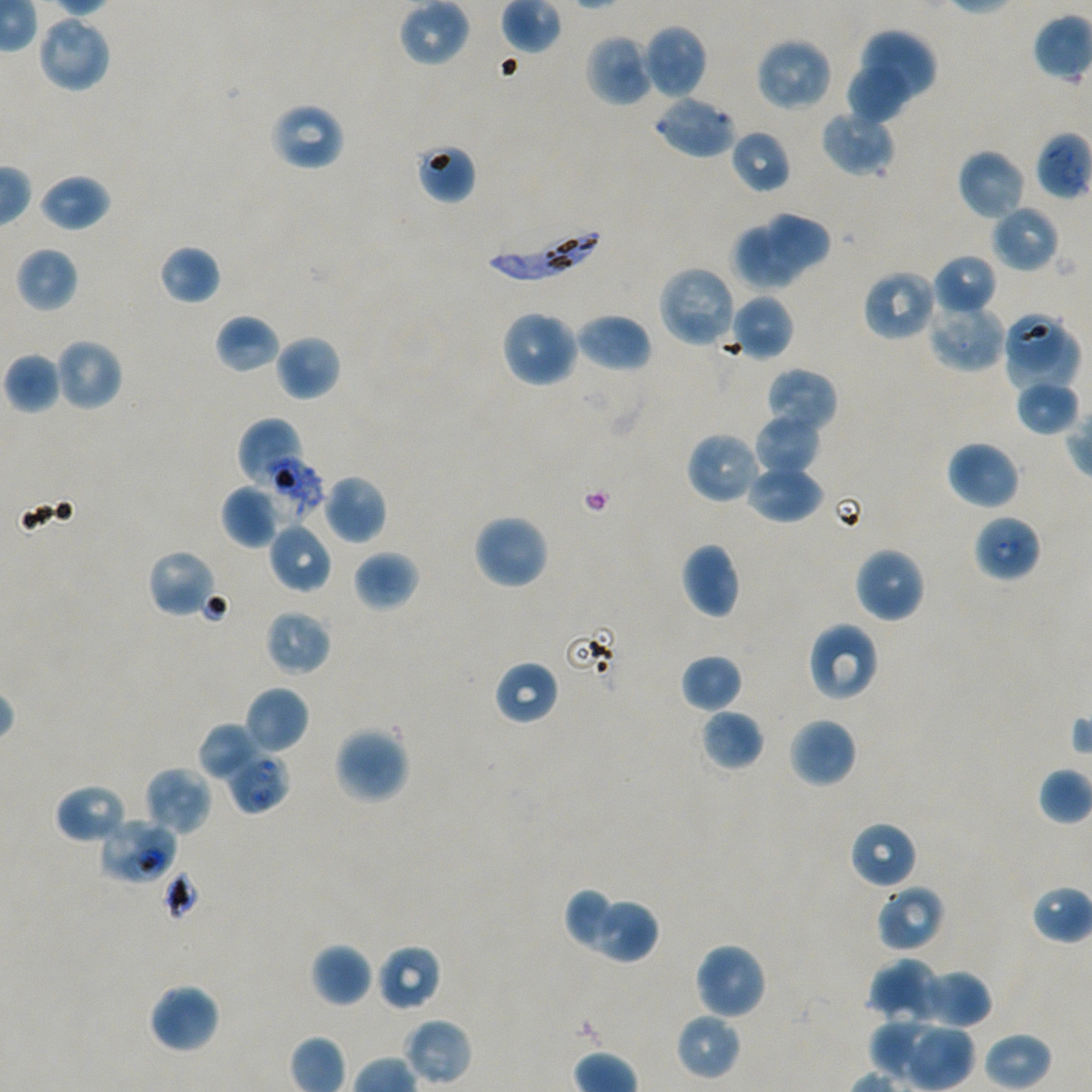
Approximate bounding rectangles given as corner coordinates in pixels from the top-left. Not every red blood cell is marked. Locations of red blood cells of indeterminate infection status: (x1=255, y1=448, x2=325, y2=522), (x1=973, y1=513, x2=1042, y2=583), (x1=227, y1=751, x2=290, y2=814), (x1=98, y1=816, x2=177, y2=885), (x1=162, y1=869, x2=202, y2=923). Locations of uninfected red blood cells: (x1=399, y1=0, x2=471, y2=67), (x1=35, y1=13, x2=113, y2=94), (x1=642, y1=24, x2=708, y2=100), (x1=856, y1=28, x2=937, y2=106), (x1=584, y1=33, x2=655, y2=108), (x1=754, y1=37, x2=833, y2=113), (x1=845, y1=58, x2=913, y2=125), (x1=653, y1=94, x2=738, y2=160), (x1=269, y1=101, x2=346, y2=172), (x1=820, y1=109, x2=896, y2=177), (x1=729, y1=129, x2=791, y2=194), (x1=415, y1=143, x2=477, y2=204), (x1=957, y1=149, x2=1026, y2=220), (x1=39, y1=173, x2=111, y2=232), (x1=991, y1=204, x2=1060, y2=273), (x1=766, y1=211, x2=833, y2=272), (x1=731, y1=225, x2=801, y2=290), (x1=158, y1=244, x2=221, y2=305), (x1=15, y1=246, x2=78, y2=312), (x1=932, y1=253, x2=997, y2=314), (x1=657, y1=265, x2=738, y2=350), (x1=861, y1=268, x2=938, y2=342), (x1=729, y1=293, x2=794, y2=361), (x1=928, y1=298, x2=1007, y2=371), (x1=500, y1=309, x2=580, y2=388), (x1=1002, y1=311, x2=1066, y2=370), (x1=574, y1=312, x2=653, y2=373), (x1=214, y1=313, x2=280, y2=374), (x1=1008, y1=327, x2=1080, y2=392), (x1=274, y1=335, x2=341, y2=401), (x1=54, y1=338, x2=124, y2=412), (x1=3, y1=351, x2=62, y2=414), (x1=765, y1=367, x2=838, y2=437), (x1=1013, y1=378, x2=1080, y2=437), (x1=754, y1=414, x2=820, y2=477), (x1=237, y1=418, x2=303, y2=492), (x1=685, y1=430, x2=763, y2=505), (x1=946, y1=440, x2=1021, y2=511), (x1=746, y1=464, x2=824, y2=524), (x1=321, y1=473, x2=388, y2=545), (x1=221, y1=484, x2=283, y2=548), (x1=472, y1=513, x2=550, y2=591), (x1=268, y1=522, x2=333, y2=594), (x1=679, y1=542, x2=742, y2=619), (x1=853, y1=546, x2=926, y2=623), (x1=147, y1=549, x2=218, y2=619), (x1=353, y1=550, x2=420, y2=612), (x1=264, y1=608, x2=332, y2=676), (x1=806, y1=621, x2=880, y2=702), (x1=680, y1=654, x2=744, y2=714), (x1=493, y1=659, x2=560, y2=726), (x1=243, y1=685, x2=310, y2=754), (x1=700, y1=708, x2=765, y2=771), (x1=788, y1=716, x2=858, y2=788), (x1=199, y1=723, x2=266, y2=782), (x1=333, y1=725, x2=410, y2=805), (x1=143, y1=765, x2=214, y2=837), (x1=1038, y1=766, x2=1092, y2=826), (x1=54, y1=783, x2=128, y2=845), (x1=850, y1=820, x2=917, y2=890), (x1=875, y1=885, x2=945, y2=953), (x1=1032, y1=885, x2=1092, y2=945), (x1=565, y1=887, x2=616, y2=949), (x1=594, y1=900, x2=659, y2=965), (x1=693, y1=941, x2=767, y2=1021), (x1=310, y1=943, x2=374, y2=1007), (x1=376, y1=945, x2=442, y2=1012), (x1=869, y1=959, x2=942, y2=1023), (x1=909, y1=968, x2=991, y2=1029), (x1=149, y1=983, x2=221, y2=1054), (x1=675, y1=1013, x2=742, y2=1080), (x1=403, y1=1018, x2=472, y2=1087), (x1=873, y1=1019, x2=943, y2=1077), (x1=902, y1=1024, x2=976, y2=1090). Locations of infected red blood cells: (x1=1035, y1=131, x2=1092, y2=200), (x1=482, y1=228, x2=602, y2=283). Oil immersion, 100x objective (numerical aperture 1.45). Giemsa stain. Plasmodium falciparum strain NF54 in static in-vitro culture. One field from this slide. Image is 1092×1092 pixels. Thin blood film. Donor blood group A+/O+.